State which parasite is depicted.
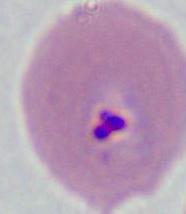

Plasmodium.

Summary:
  - Modality: photomicrograph
  - Magnification: 400x or 1000x